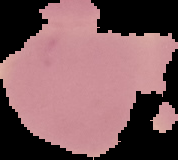
Summary:
  - Image type: segmented cell region on a black background
  - Result: no malaria parasites seen
  - Preparation: thin blood film
  - Image size: 178×160 pixels